Give the position of every leukocyte visible.
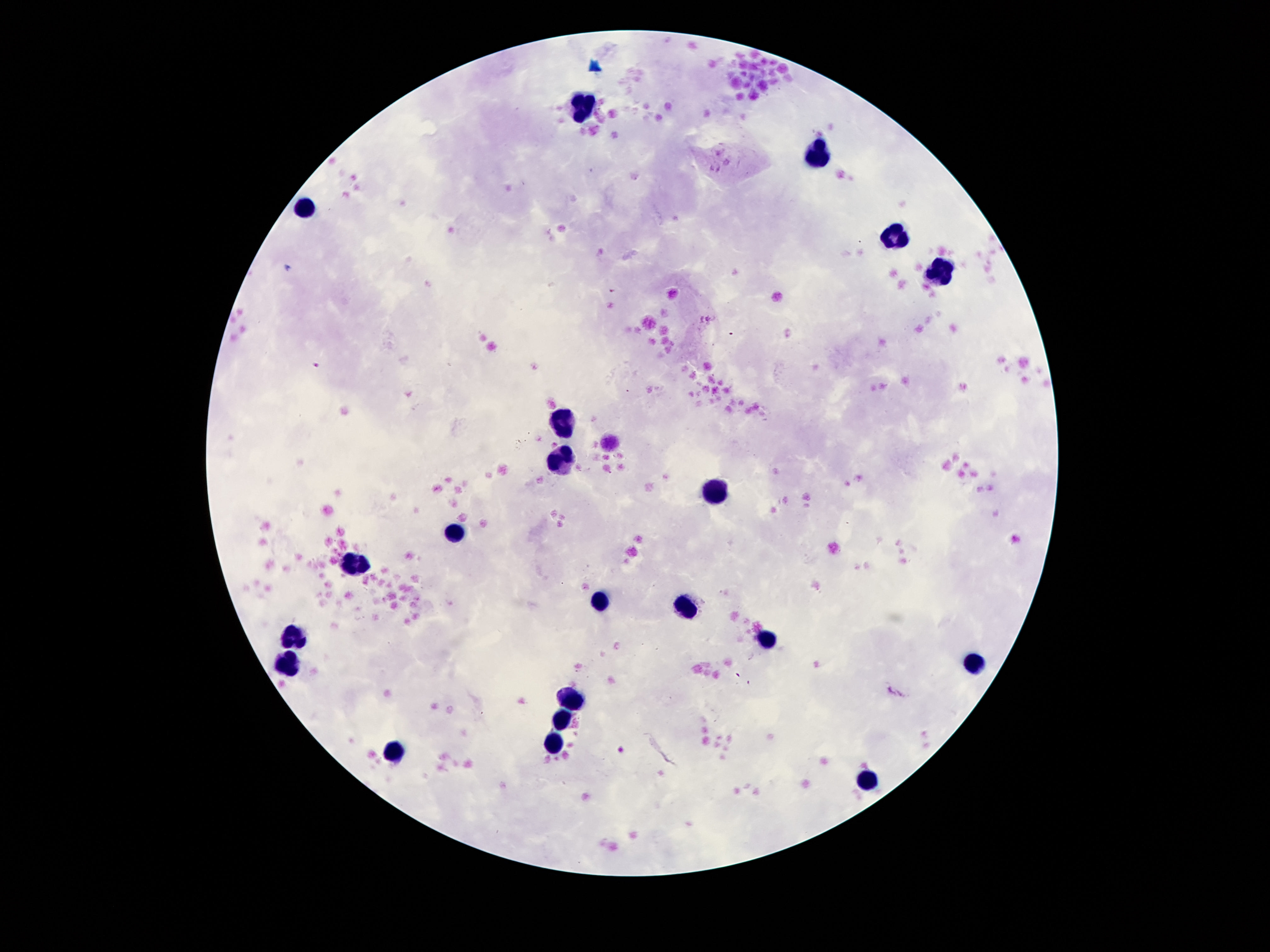
Approximate centers as {x, y} in pixels.
Leukocytes: {580, 109}, {817, 157}, {306, 207}, {894, 240}, {942, 272}, {563, 416}, {563, 462}, {719, 490}, {457, 534}, {356, 559}, {599, 598}, {685, 608}, {291, 637}, {769, 639}, {287, 663}, {973, 663}, {570, 699}, {560, 720}, {556, 747}, {392, 753}, {868, 778}.

100x magnification. Patient malaria status: negative. One field from this slide. Thick peripheral-blood smear. Giemsa-stained preparation. Image is 1270×952 pixels. Photographed through the microscope eyepiece with a smartphone camera.